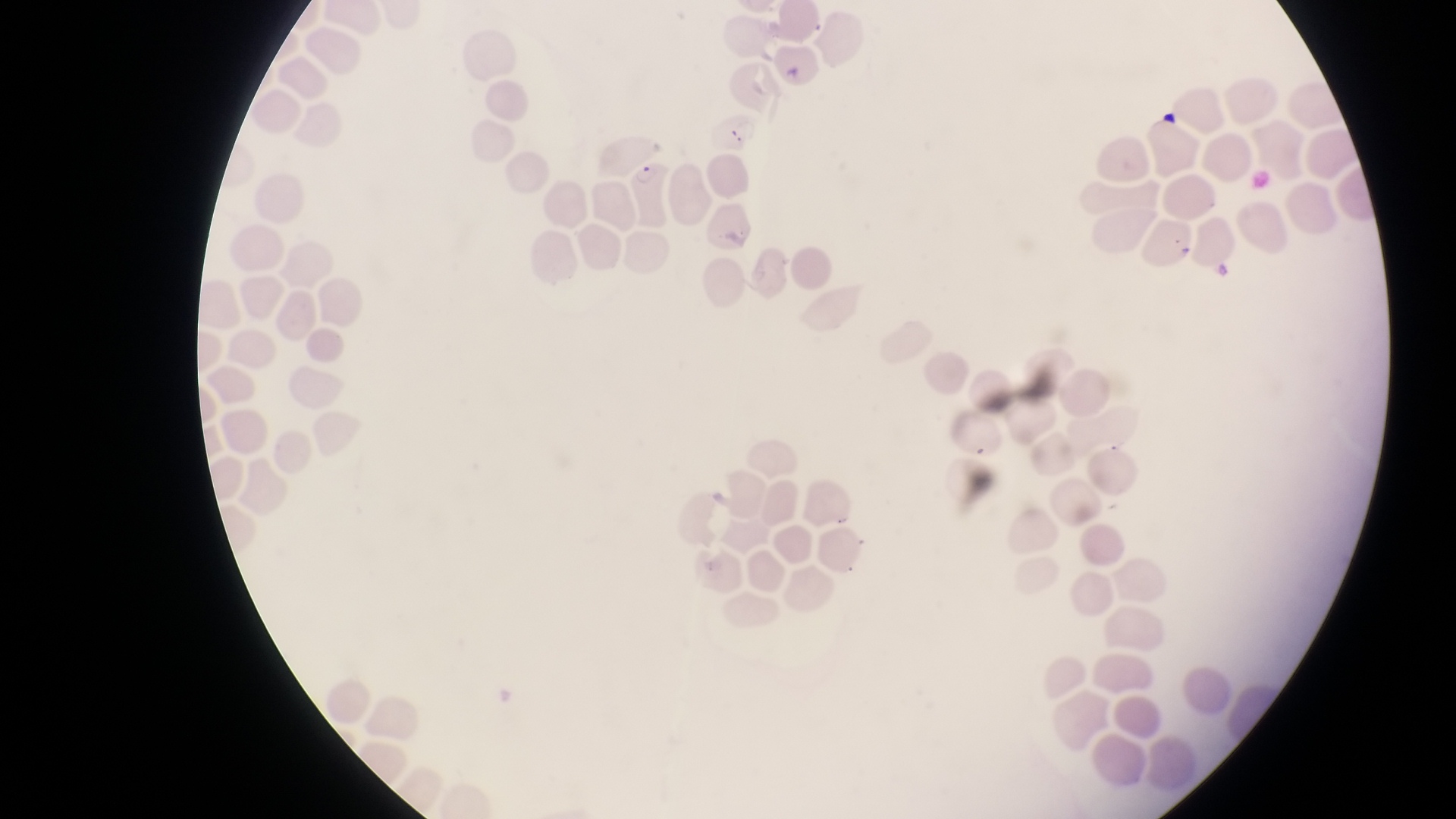
{
  "preparation": "thin blood smear",
  "field_of_view": "single",
  "capture": "smartphone photograph through the eyepiece of an Olympus CX-23 microscope",
  "magnification": "1000x",
  "image_size": "1456×819 pixels",
  "country": "Uganda",
  "artifact_platelet_like_body_stain_precipitate_or_debris_locations": "approximate bounding boxes as {left, top, right, bottom} in pixels: {1160, 103, 1181, 132}",
  "parasitised_red_blood_cell_locations": "approximate bounding boxes as {left, top, right, bottom} in pixels: {711, 112, 764, 157}, {629, 158, 675, 225}"
}